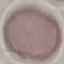

result = no malaria parasites seen
preparation = thin blood smear
capture = smartphone camera at the microscope eyepiece
image type = automatically extracted cell patch, resized to 64 × 64 pixels
stain = Giemsa